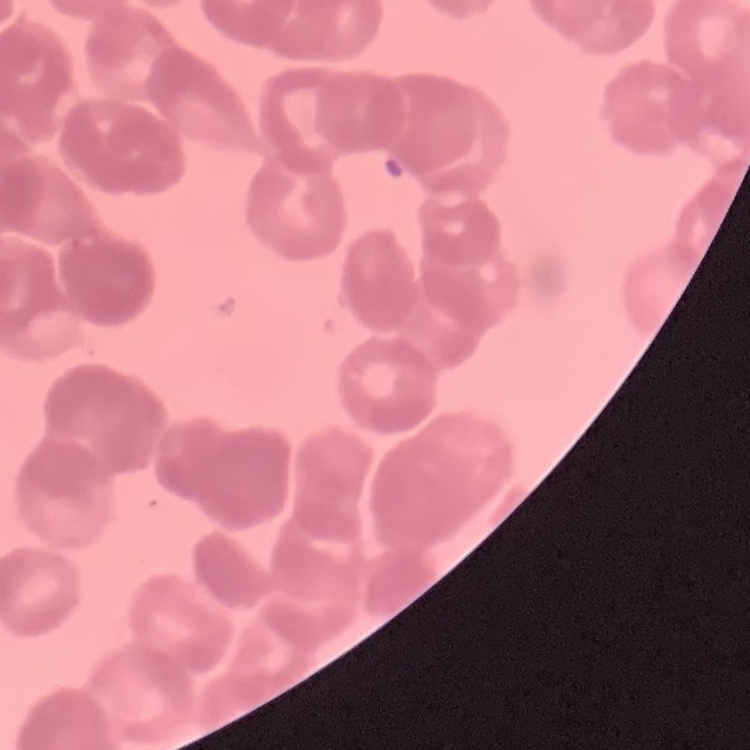

The erythrocytes show rouleaux formation. Thin blood smear. One tile cut from a larger photomicrograph. Field's or Giemsa stain.